Locate and identify every blood parasite.
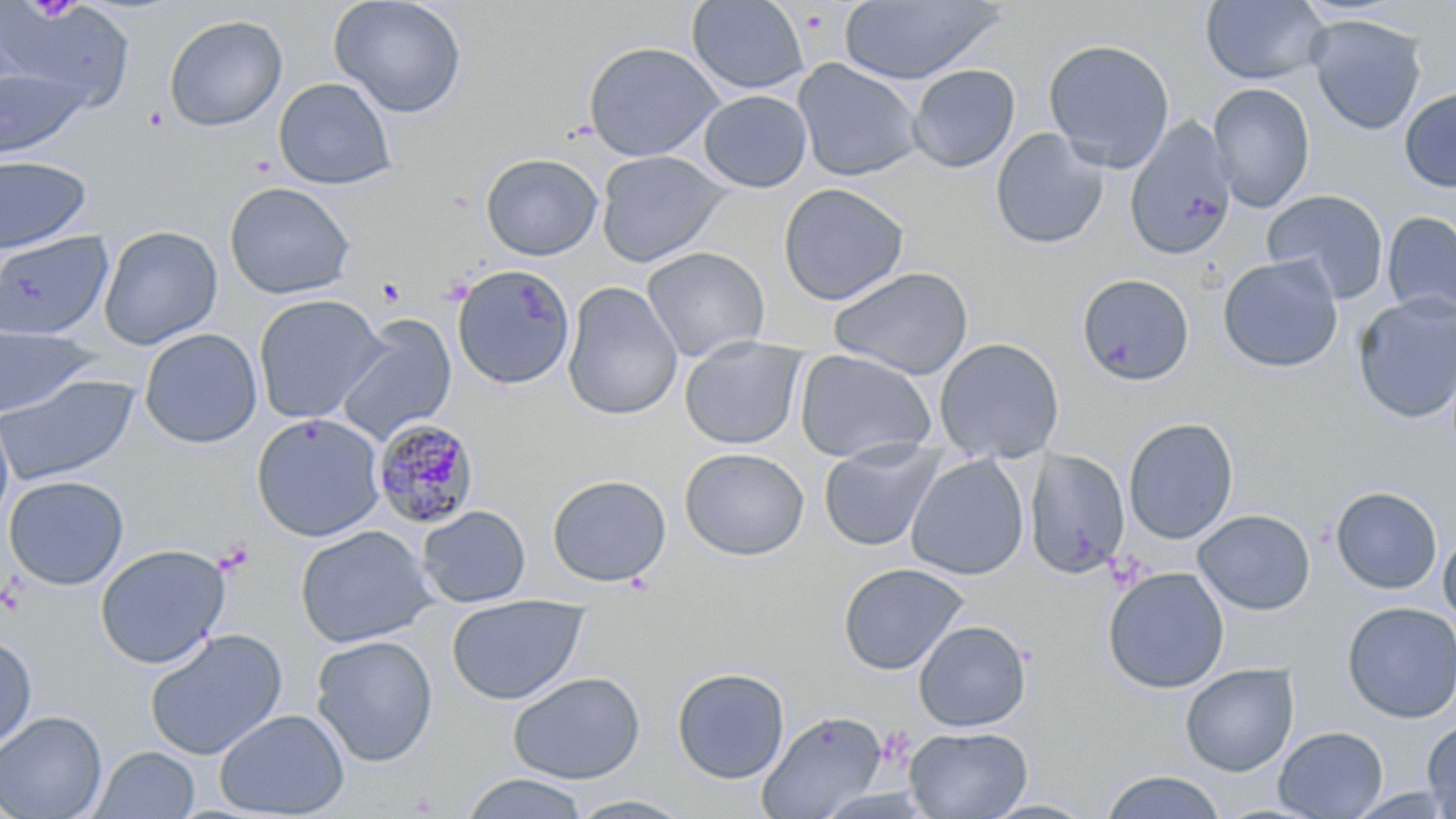

Approximate bounding boxes as named x1/y1/x2/y2 corners in pixels.
Plasmodium malariae-infected red blood cells: (x1=372, y1=419, x2=481, y2=529).
No Plasmodium falciparum, Plasmodium ovale, Plasmodium vivax, Babesia divergens, or Trypanosoma brucei observed.

Summary:
  - Platelet locations: (x1=876, y1=726, x2=915, y2=767)
  - Uninfected red blood cell locations: (x1=329, y1=0, x2=468, y2=118), (x1=687, y1=0, x2=810, y2=95), (x1=1200, y1=0, x2=1329, y2=85), (x1=839, y1=1, x2=1003, y2=85), (x1=1, y1=2, x2=136, y2=115), (x1=163, y1=14, x2=288, y2=132), (x1=1305, y1=14, x2=1428, y2=135), (x1=1042, y1=38, x2=1176, y2=171), (x1=583, y1=41, x2=724, y2=161), (x1=793, y1=58, x2=922, y2=182), (x1=1, y1=64, x2=91, y2=160), (x1=907, y1=64, x2=1020, y2=173), (x1=273, y1=77, x2=397, y2=189), (x1=1208, y1=82, x2=1315, y2=212), (x1=1398, y1=87, x2=1456, y2=193), (x1=698, y1=90, x2=812, y2=193), (x1=1124, y1=117, x2=1237, y2=261), (x1=990, y1=128, x2=1109, y2=250), (x1=595, y1=150, x2=731, y2=267), (x1=481, y1=152, x2=603, y2=260), (x1=0, y1=155, x2=92, y2=253), (x1=224, y1=182, x2=356, y2=300), (x1=778, y1=183, x2=910, y2=305), (x1=1262, y1=189, x2=1389, y2=304), (x1=1381, y1=210, x2=1456, y2=320), (x1=99, y1=225, x2=223, y2=350), (x1=0, y1=231, x2=113, y2=341), (x1=641, y1=246, x2=771, y2=363), (x1=1217, y1=254, x2=1344, y2=373), (x1=451, y1=264, x2=576, y2=390), (x1=828, y1=266, x2=974, y2=380), (x1=1076, y1=272, x2=1195, y2=386), (x1=561, y1=281, x2=683, y2=421), (x1=1351, y1=293, x2=1456, y2=424), (x1=252, y1=294, x2=388, y2=424), (x1=335, y1=316, x2=457, y2=447), (x1=0, y1=322, x2=99, y2=418), (x1=139, y1=327, x2=263, y2=449), (x1=679, y1=335, x2=806, y2=450), (x1=933, y1=337, x2=1065, y2=463), (x1=794, y1=348, x2=938, y2=464), (x1=0, y1=373, x2=138, y2=487), (x1=0, y1=406, x2=15, y2=530), (x1=251, y1=412, x2=386, y2=542), (x1=1123, y1=417, x2=1238, y2=544), (x1=818, y1=440, x2=944, y2=552), (x1=679, y1=447, x2=809, y2=561), (x1=1025, y1=448, x2=1130, y2=578), (x1=906, y1=453, x2=1029, y2=580), (x1=546, y1=473, x2=671, y2=588), (x1=2, y1=475, x2=129, y2=590), (x1=1331, y1=486, x2=1443, y2=595), (x1=417, y1=505, x2=531, y2=608), (x1=1193, y1=508, x2=1315, y2=615), (x1=294, y1=525, x2=438, y2=648), (x1=1438, y1=529, x2=1456, y2=627), (x1=94, y1=543, x2=231, y2=669), (x1=838, y1=562, x2=969, y2=675), (x1=1103, y1=566, x2=1229, y2=694), (x1=446, y1=594, x2=588, y2=705), (x1=1341, y1=601, x2=1456, y2=724), (x1=913, y1=619, x2=1032, y2=732), (x1=144, y1=627, x2=288, y2=761), (x1=0, y1=632, x2=37, y2=753), (x1=311, y1=634, x2=438, y2=767), (x1=1180, y1=663, x2=1299, y2=776), (x1=671, y1=666, x2=791, y2=784), (x1=508, y1=671, x2=646, y2=784), (x1=214, y1=708, x2=350, y2=818), (x1=0, y1=710, x2=107, y2=819), (x1=757, y1=710, x2=889, y2=818), (x1=1421, y1=720, x2=1456, y2=817), (x1=904, y1=725, x2=1032, y2=818), (x1=1274, y1=726, x2=1388, y2=818), (x1=91, y1=746, x2=200, y2=818), (x1=1100, y1=770, x2=1227, y2=819), (x1=460, y1=773, x2=589, y2=819), (x1=566, y1=794, x2=697, y2=818), (x1=979, y1=798, x2=1099, y2=818)
  - Slide-level diagnosis: Plasmodium malariae
  - Modality: optical microscopy
  - Magnification: 1000x
  - Preparation: thin blood smear
  - Image size: 1456×819 pixels
  - Field of view: single
  - Stain: May-Grünwald-Giemsa